Classify this cell by malaria status.
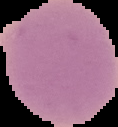
It is uninfected.

Summary:
  - Image type: segmented cell region on a black background
  - Preparation: thin blood film
  - Image size: 118×127 pixels